Report the malaria status of this cell.
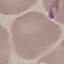
It is parasitized.

preparation: thin blood smear
stain: Giemsa
image_type: automatically extracted cell patch, resized to 64 × 64 pixels
capture: smartphone through the microscope eyepiece